Classify this cell by malaria status.
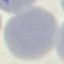

Uninfected.

Summary:
  - Capture: smartphone camera at the microscope eyepiece
  - Stain: Giemsa
  - Image type: automatically extracted cell patch, resized to 64 × 64 pixels
  - Preparation: thin smear